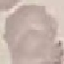
Malaria status: uninfected. Cell patch, automatically extracted from a larger field of view and resized to 64 × 64 pixels. Giemsa-stained preparation. Acquired by smartphone through the microscope eyepiece. Thin blood film.